Assess this cell for malaria.
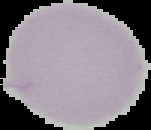

Uninfected.

Image is 151×130 pixels. From a thin blood film. Cell region segmented out of the field of view; the surrounding area is masked to black.